Locate every Plasmodium malariae-infected red blood cell.
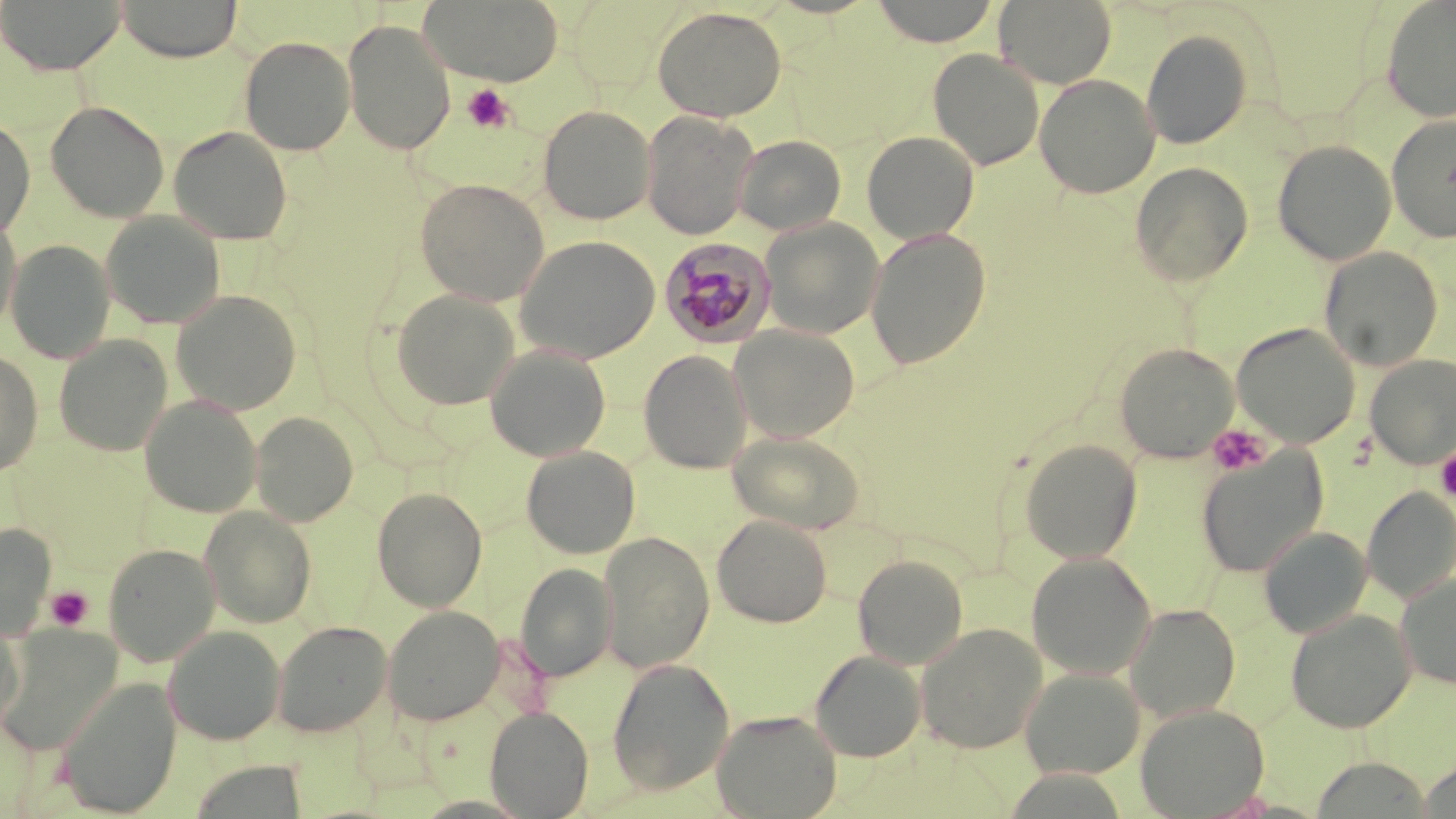
Approximate bounding boxes as (x1,y1)-(x2,y2) corner pairs in pixels.
Plasmodium malariae-infected red blood cells: (659,240)-(778,350).

{
  "slide_level_diagnosis": "Plasmodium malariae",
  "modality": "light microscopy",
  "image_size": "1456×819 pixels",
  "platelet_locations": "approximate bounding boxes as (x1,y1)-(x2,y2) corner pairs in pixels: (463,84)-(513,133), (1207,424)-(1270,476), (1435,445)-(1456,504), (46,586)-(93,631)",
  "uninfected_red_blood_cell_locations": "approximate bounding boxes as (x1,y1)-(x2,y2) corner pairs in pixels: (1,0)-(126,75), (115,0)-(242,62), (420,0)-(564,85), (869,0)-(1001,47), (994,0)-(1116,89), (1381,0)-(1456,122), (652,6)-(786,122), (342,20)-(455,155), (1141,28)-(1253,149), (239,35)-(356,155), (928,49)-(1044,170), (1034,73)-(1160,198), (45,100)-(169,223), (538,105)-(655,225), (641,110)-(756,239), (1386,113)-(1456,243), (0,116)-(35,239), (168,126)-(292,245), (862,131)-(979,244), (734,134)-(846,235), (1273,140)-(1396,265), (1130,161)-(1253,287), (414,178)-(550,306), (101,212)-(226,329), (760,218)-(884,339), (0,220)-(21,335), (866,228)-(990,370), (514,235)-(660,363), (5,240)-(115,363), (1319,247)-(1444,371), (389,288)-(520,410), (170,290)-(302,415), (1231,323)-(1361,448), (730,325)-(860,442), (54,335)-(173,457), (1115,342)-(1238,463), (485,344)-(611,462), (0,350)-(43,477), (638,350)-(752,474), (1365,354)-(1456,468), (140,395)-(263,517), (250,411)-(358,527), (727,429)-(865,535), (1019,439)-(1142,564), (521,446)-(640,559), (1197,447)-(1327,578), (372,486)-(487,612), (1362,486)-(1456,604), (199,506)-(316,628), (712,514)-(832,627), (0,522)-(56,640), (1259,526)-(1373,639), (598,531)-(715,673), (102,543)-(220,666), (1026,552)-(1157,680), (853,554)-(968,669), (515,562)-(617,682), (1396,573)-(1456,690), (1125,604)-(1240,722), (383,605)-(504,726), (1285,609)-(1416,733), (0,612)-(24,734), (272,620)-(391,737), (915,622)-(1048,753), (0,624)-(122,754), (164,626)-(285,745), (810,650)-(926,762), (607,657)-(735,796), (1020,667)-(1145,780), (56,677)-(181,817), (1135,703)-(1270,818), (485,706)-(594,818), (711,709)-(842,819), (1310,757)-(1434,817), (189,761)-(310,818)",
  "field_of_view": "single",
  "magnification": "1000x",
  "stain": "May-Grünwald-Giemsa",
  "preparation": "thin blood smear"
}